Outline each blood parasite and name the species.
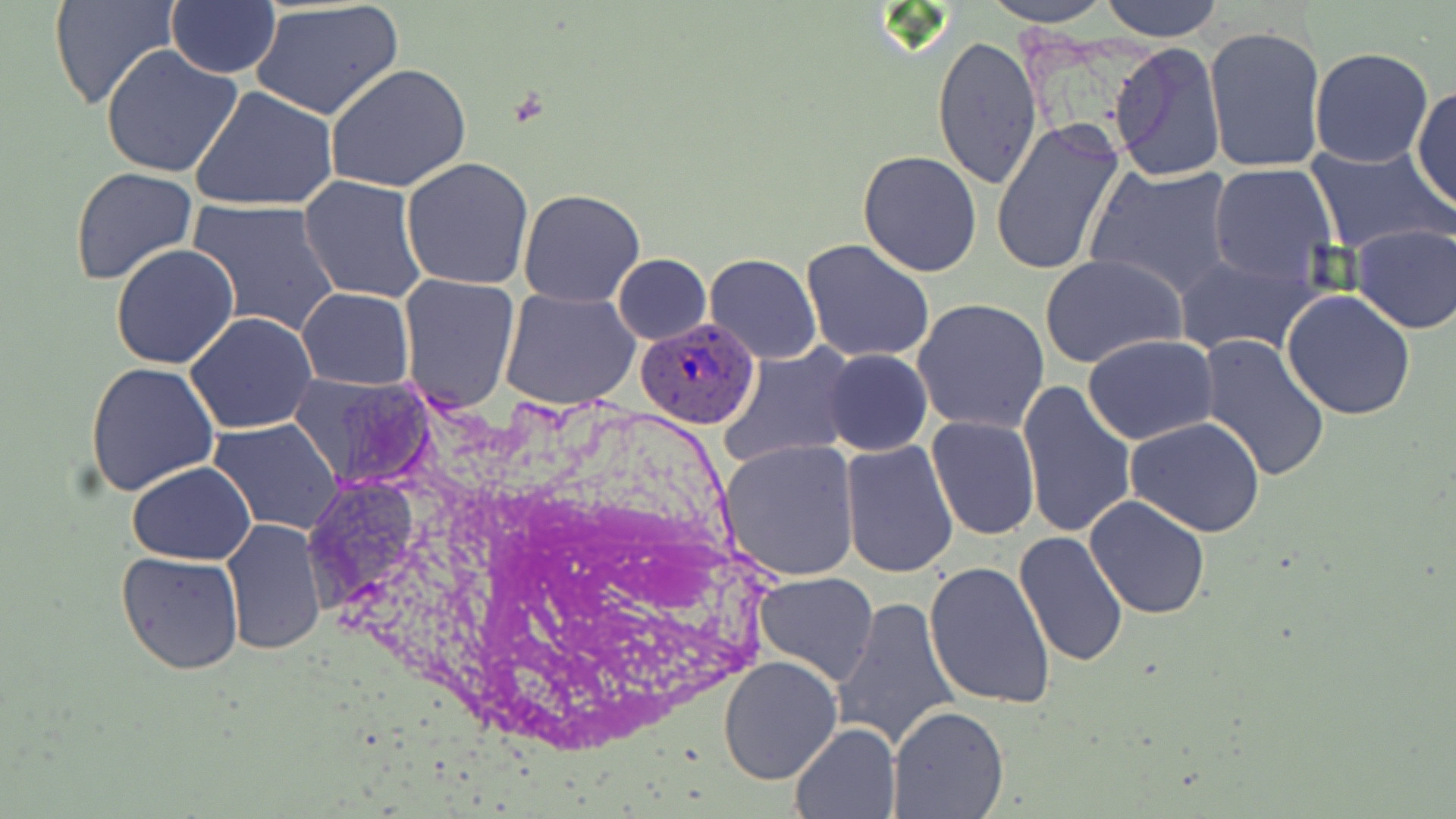
Approximate bounding boxes as (x1, y1, x2, y2) in pixels.
Plasmodium ovale-infected red blood cells: (635, 315, 762, 432).
No Plasmodium falciparum, Plasmodium malariae, Plasmodium vivax, Babesia divergens, or Trypanosoma brucei observed.

Uninfected red blood cell locations: (51, 0, 180, 113), (981, 0, 1116, 26), (1099, 0, 1225, 41), (166, 1, 282, 76), (250, 2, 404, 121), (1204, 24, 1329, 173), (932, 33, 1042, 189), (1108, 39, 1226, 180), (98, 43, 244, 178), (1308, 46, 1433, 169), (326, 63, 473, 195), (1411, 82, 1456, 213), (191, 86, 338, 211), (990, 120, 1125, 278), (1303, 144, 1452, 254), (858, 151, 983, 277), (401, 156, 533, 289), (1084, 162, 1236, 300), (1209, 164, 1337, 287), (70, 166, 198, 286), (299, 176, 425, 304), (517, 189, 645, 308), (186, 197, 342, 339), (1348, 223, 1456, 335), (800, 238, 935, 365), (110, 244, 240, 369), (611, 253, 711, 344), (703, 253, 822, 365), (1039, 254, 1187, 369), (1173, 254, 1323, 358), (398, 274, 522, 412), (297, 288, 414, 388), (500, 288, 639, 410), (1281, 290, 1416, 420), (913, 299, 1050, 433), (185, 311, 317, 434), (1197, 333, 1331, 481), (1083, 334, 1217, 444), (720, 345, 855, 470), (823, 348, 932, 457), (85, 362, 220, 498), (287, 371, 438, 491), (1017, 380, 1136, 539), (925, 414, 1040, 541), (1124, 417, 1267, 537), (210, 419, 343, 533), (717, 438, 861, 582), (839, 440, 959, 578), (127, 462, 257, 564), (1085, 495, 1210, 619), (221, 519, 327, 656), (1011, 530, 1128, 669), (115, 551, 245, 675), (924, 559, 1058, 711), (753, 572, 879, 687), (835, 597, 961, 754), (719, 656, 843, 784), (887, 706, 1009, 819), (790, 721, 902, 818). Slide-level diagnosis: Plasmodium ovale. Image is 1456×819 pixels. Light microscopy. 1000x magnification. May-Grünwald-Giemsa-stained preparation. Thin blood film. Single field of view.